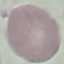
malaria_status: uninfected
stain: Giemsa
capture: smartphone camera at the microscope eyepiece
preparation: thin smear
image_type: automatically extracted cell patch, resized to 64 × 64 pixels